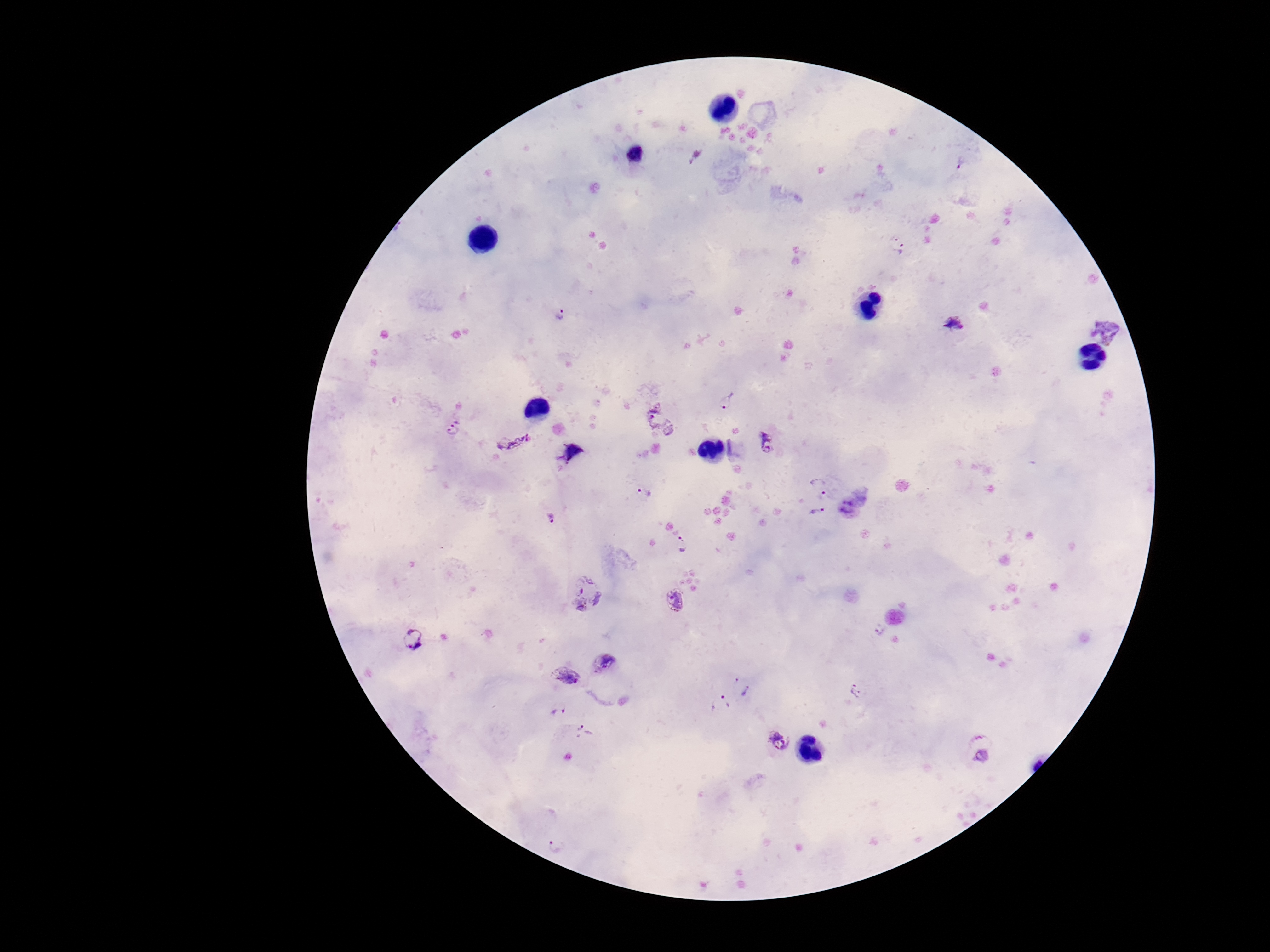
field of view = one from this slide
image size = 1270×952 pixels
capture = smartphone camera through the microscope eyepiece
patient malaria status = infected
magnification = 100x
preparation = thick blood smear
Plasmodium parasite locations = approximate centers as (x, y) in pixels: (962, 165), (898, 242), (560, 314), (955, 324), (1106, 329), (727, 399), (660, 418), (454, 419), (452, 434), (514, 442), (769, 443), (819, 486), (644, 492), (819, 514), (552, 518), (682, 544), (588, 593), (675, 600), (879, 629), (414, 639), (604, 662), (569, 675), (855, 689), (748, 692), (722, 704), (559, 712), (585, 733), (778, 742), (981, 746), (558, 844)
stain = Giemsa